Give the extent of all Plasmodium falciparum-infected red blood cells.
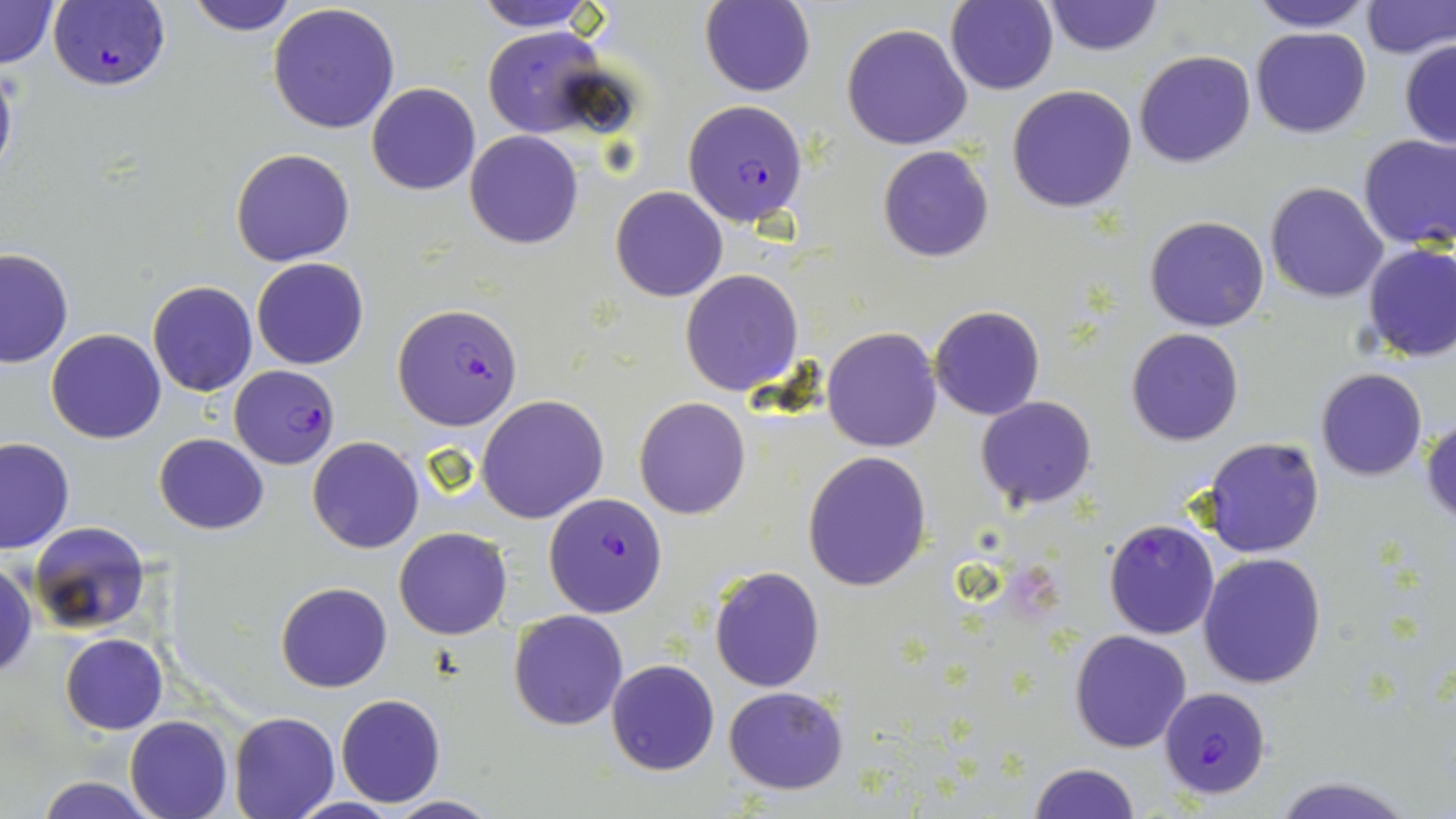
Approximate bounding boxes as (x1, y1, x2, y2) in pixels.
Plasmodium falciparum-infected red blood cells: (46, 2, 171, 93), (683, 99, 810, 227), (391, 303, 523, 428), (231, 364, 340, 468), (544, 491, 669, 617), (1158, 687, 1271, 800).

Uninfected red blood cell locations: (0, 0, 61, 69), (186, 0, 299, 34), (473, 0, 603, 31), (1042, 0, 1164, 57), (1246, 0, 1375, 33), (700, 1, 816, 97), (945, 1, 1058, 93), (1360, 1, 1455, 58), (267, 4, 400, 134), (842, 22, 973, 151), (482, 27, 615, 140), (1250, 27, 1371, 138), (1399, 38, 1456, 148), (1133, 50, 1255, 168), (0, 58, 18, 193), (366, 82, 481, 196), (1007, 84, 1138, 213), (464, 131, 582, 248), (1357, 134, 1456, 251), (231, 147, 355, 267), (878, 147, 995, 262), (1264, 181, 1388, 302), (610, 186, 727, 301), (1145, 215, 1270, 333), (1361, 244, 1456, 364), (0, 248, 74, 368), (252, 258, 369, 370), (680, 270, 802, 395), (148, 280, 257, 396), (930, 306, 1044, 421), (822, 327, 941, 451), (1126, 328, 1245, 447), (45, 329, 165, 444), (1315, 368, 1427, 481), (476, 394, 607, 523), (975, 396, 1099, 511), (634, 397, 749, 519), (1423, 415, 1456, 526), (154, 433, 269, 534), (0, 437, 74, 554), (308, 437, 423, 554), (1203, 438, 1324, 558), (803, 451, 931, 592), (1102, 518, 1219, 640), (30, 521, 151, 634), (395, 527, 511, 640), (1199, 552, 1328, 689), (0, 561, 37, 681), (709, 566, 825, 692), (275, 581, 393, 692), (508, 609, 629, 730), (1069, 629, 1193, 753), (61, 632, 166, 734), (607, 659, 719, 775), (723, 686, 848, 795), (336, 695, 445, 806), (228, 711, 339, 818), (124, 715, 232, 819), (1028, 763, 1141, 818), (1267, 774, 1417, 819), (31, 776, 163, 818), (384, 795, 502, 818). Slide-level diagnosis: Plasmodium falciparum. Light microscopy. May-Grünwald-Giemsa stain. Single field of view. Captured at 1000x magnification. Thin blood smear. Image is 1456×819 pixels.